Locate leukocytes (white blood cells).
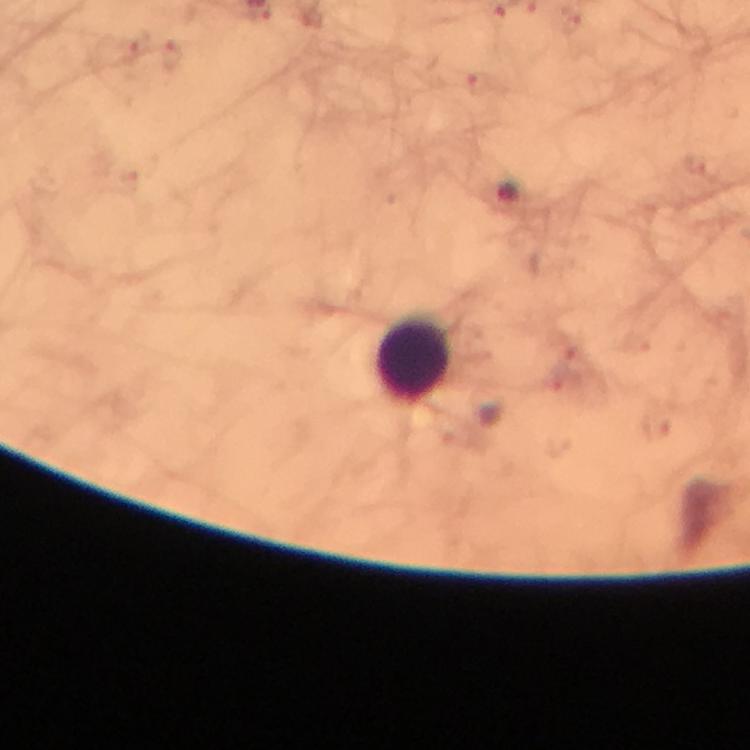
Approximate centers as (x, y) in pixels.
Leukocytes: (413, 360).

capture: smartphone camera through the microscope
context: from a malaria diagnostic workup
preparation: thick blood smear
immersion_oil: applied
magnification: 100x
cropped_from: a single field of view
image_size: 750×750 pixels
plasmodium_parasite_locations: 'approximate centers as (x, y) in pixels: (171, 56), (477, 85), (656, 428)'
stain: Giemsa